Locate every uninfected red blood cell.
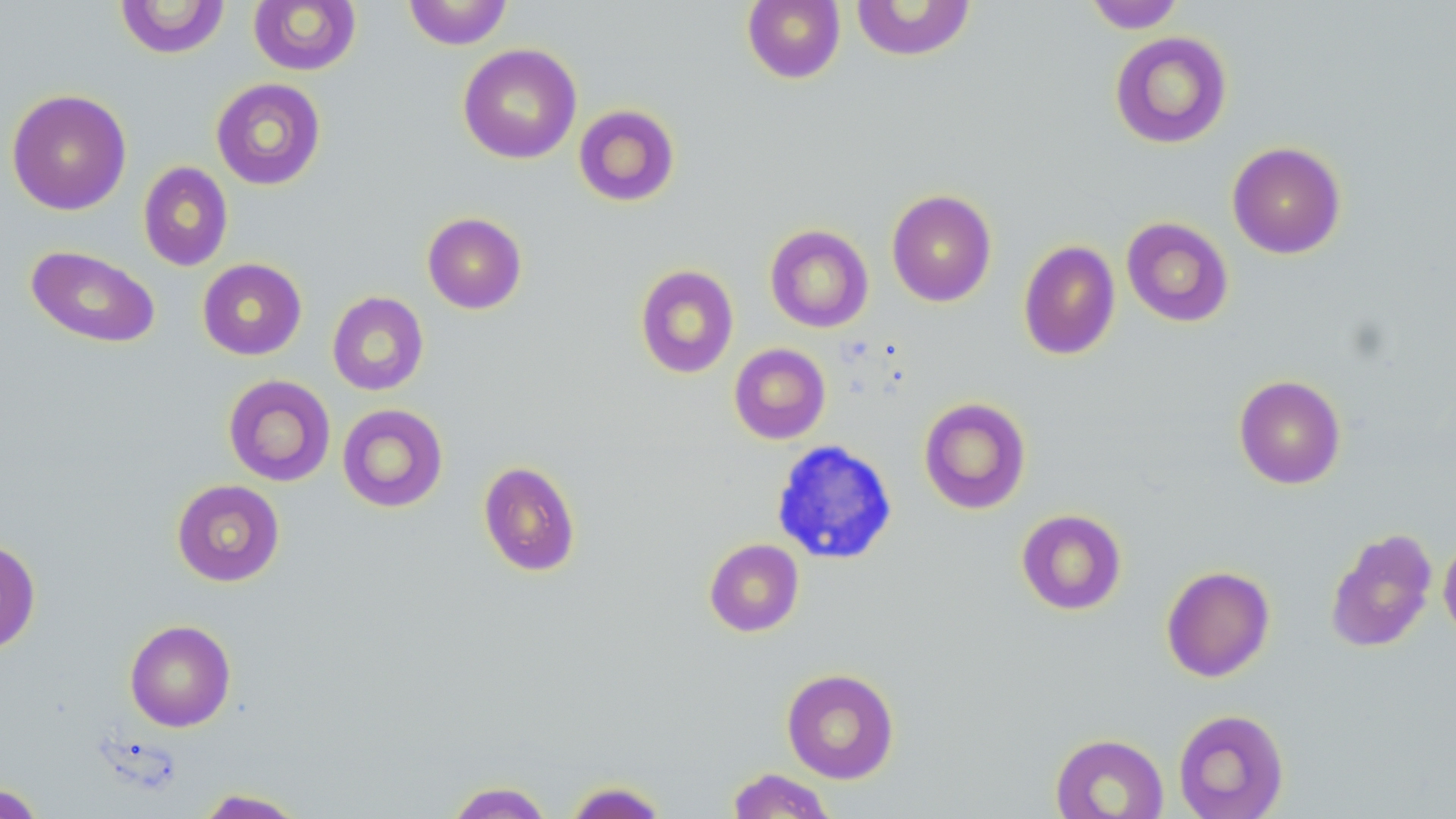
Approximate bounding boxes as [x1, y1, x2, y2] in pixels.
Uninfected red blood cells: [115, 0, 230, 59], [403, 0, 513, 49], [742, 0, 845, 84], [248, 1, 361, 75], [850, 1, 977, 61], [1084, 1, 1185, 33], [1109, 31, 1233, 149], [458, 43, 582, 164], [210, 77, 326, 190], [6, 88, 132, 216], [573, 104, 680, 207], [1227, 141, 1346, 259], [138, 162, 233, 271], [886, 189, 997, 307], [422, 212, 527, 314], [1121, 217, 1234, 327], [764, 224, 873, 333], [1018, 240, 1121, 360], [25, 245, 161, 349], [197, 258, 307, 360], [635, 264, 739, 379], [327, 291, 429, 396], [729, 343, 831, 445], [223, 374, 336, 486], [1234, 374, 1346, 489], [918, 396, 1032, 515], [337, 403, 449, 513], [478, 461, 581, 577], [171, 479, 286, 587], [1016, 509, 1127, 616], [1325, 527, 1439, 653], [1438, 536, 1456, 643], [0, 538, 41, 654], [704, 538, 804, 637], [1161, 565, 1275, 682], [124, 619, 236, 732], [781, 668, 899, 783], [1172, 708, 1289, 819], [1050, 732, 1169, 818], [726, 768, 837, 818], [444, 781, 554, 819], [563, 781, 669, 818], [0, 783, 46, 818], [193, 788, 308, 818].

Slide-level diagnosis: no evidence of blood parasites. One field of a larger specimen. Light microscopy. Image is 1456×819 pixels. Captured at 1000x magnification. May-Grünwald-Giemsa-stained preparation. Thin blood smear.